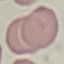
malaria_status: uninfected
preparation: thin blood film
stain: Giemsa
image_type: cell patch, automatically extracted from a larger field of view and resized to 64 × 64 pixels
capture: smartphone through the microscope eyepiece